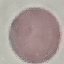

malaria_status: uninfected
image_type: cell patch, automatically extracted from a larger field of view and resized to 64 × 64 pixels
preparation: thin blood smear
stain: Giemsa
capture: smartphone through the microscope eyepiece